Classify this cell by malaria status.
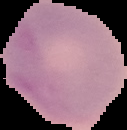
Uninfected.

Summary:
  - Preparation: thin blood smear
  - Image size: 127×130 pixels
  - Image type: segmented cell region with the area outside set to black